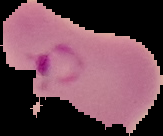

image size = 163×136 pixels
result = malaria parasites identified
image type = segmented cell region with the area outside set to black
preparation = thin blood smear